State which parasite is depicted.
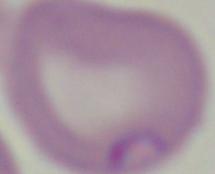
Babesia.

Micrograph. Captured at 1000x magnification.